Report the malaria status of this cell.
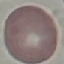

It is uninfected.

preparation = thin smear
stain = Giemsa
capture = smartphone camera at the microscope eyepiece
image type = automatically extracted cell patch, resized to 64 × 64 pixels